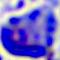
magnification = 400x
identification = white blood cell
modality = micrograph